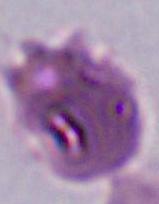
identification = Plasmodium
magnification = 400x or 1000x
modality = micrograph